Give the extent of all Plasmodium malariae-infected red blood cells.
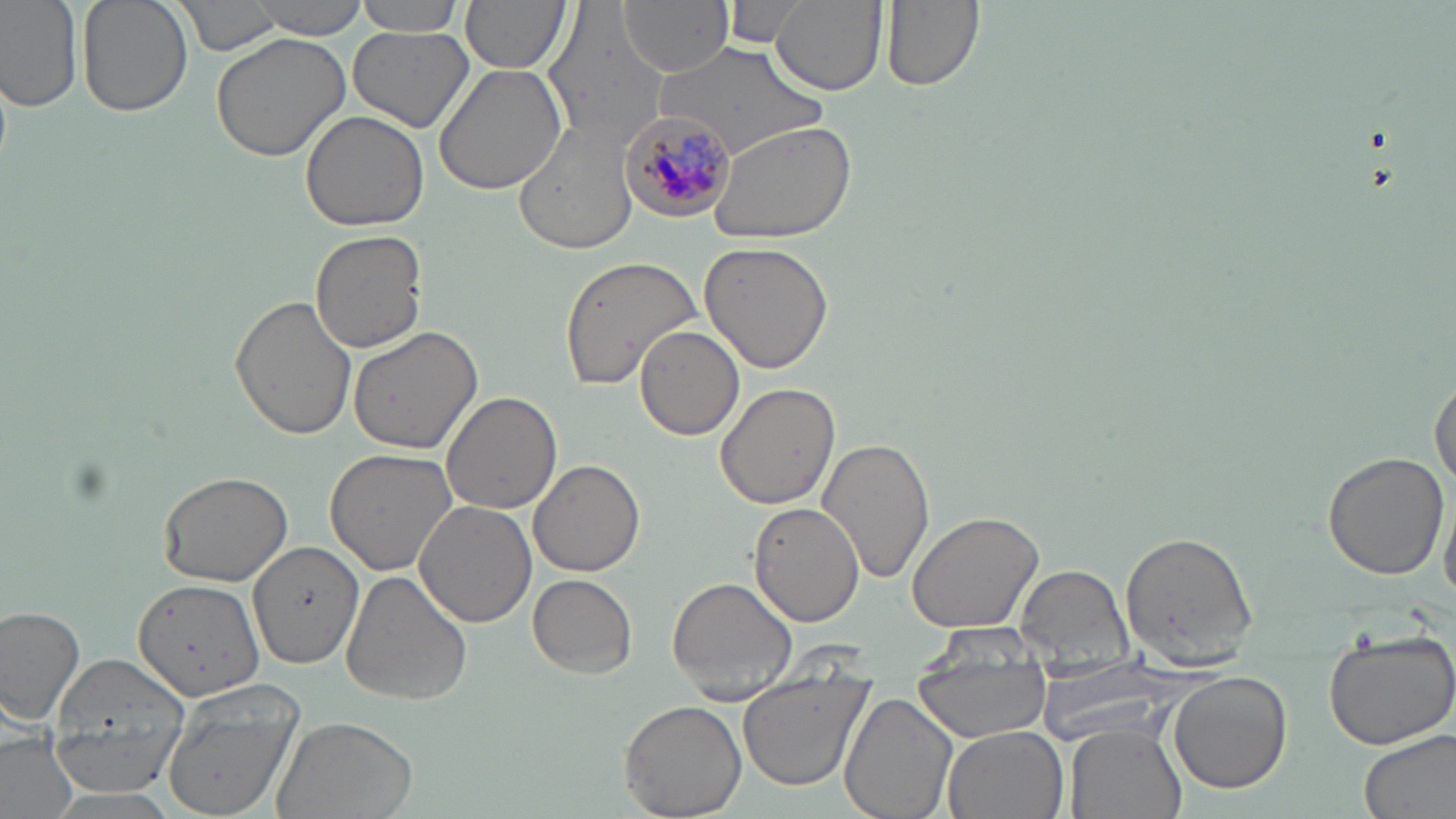

Approximate bounding boxes as [x1, y1, x2, y2] in pixels.
Plasmodium malariae-infected red blood cells: [620, 112, 739, 224].

slide-level diagnosis = Plasmodium malariae
modality = optical microscopy
uninfected red blood cell locations = approximate bounding boxes as [x1, y1, x2, y2] in pixels: [78, 0, 192, 118], [169, 0, 286, 55], [246, 0, 372, 39], [350, 0, 472, 35], [460, 0, 573, 75], [620, 0, 733, 76], [721, 0, 807, 47], [770, 0, 887, 98], [881, 0, 983, 92], [0, 1, 83, 114], [544, 8, 670, 144], [348, 25, 474, 134], [210, 30, 353, 162], [655, 43, 829, 156], [433, 61, 571, 196], [299, 107, 429, 231], [514, 119, 639, 254], [707, 120, 858, 245], [310, 230, 427, 353], [699, 240, 837, 374], [557, 255, 702, 392], [229, 295, 356, 441], [347, 325, 482, 455], [635, 325, 745, 440], [1431, 373, 1455, 491], [715, 383, 840, 511], [441, 391, 563, 514], [818, 436, 935, 587], [325, 447, 463, 577], [1321, 451, 1447, 581], [529, 459, 645, 578], [157, 466, 295, 587], [1440, 484, 1456, 602], [414, 501, 537, 629], [749, 502, 864, 626], [905, 508, 1046, 633], [1119, 531, 1261, 665], [250, 540, 364, 667], [1016, 564, 1134, 667], [339, 571, 472, 706], [528, 574, 637, 678], [666, 575, 798, 699], [132, 579, 265, 698], [1, 605, 84, 728], [913, 623, 1053, 670], [1321, 634, 1456, 753], [45, 651, 192, 795], [1035, 663, 1192, 750], [1167, 670, 1293, 794], [914, 671, 1052, 739], [738, 681, 870, 790], [158, 685, 302, 819], [840, 694, 960, 819], [619, 701, 748, 818], [270, 713, 421, 819], [1065, 725, 1185, 819], [942, 726, 1069, 819], [0, 727, 77, 819], [1359, 728, 1456, 819]
image size = 1456×819 pixels
magnification = 1000x
stain = May-Grünwald-Giemsa
field of view = one of a larger specimen
preparation = thin blood film